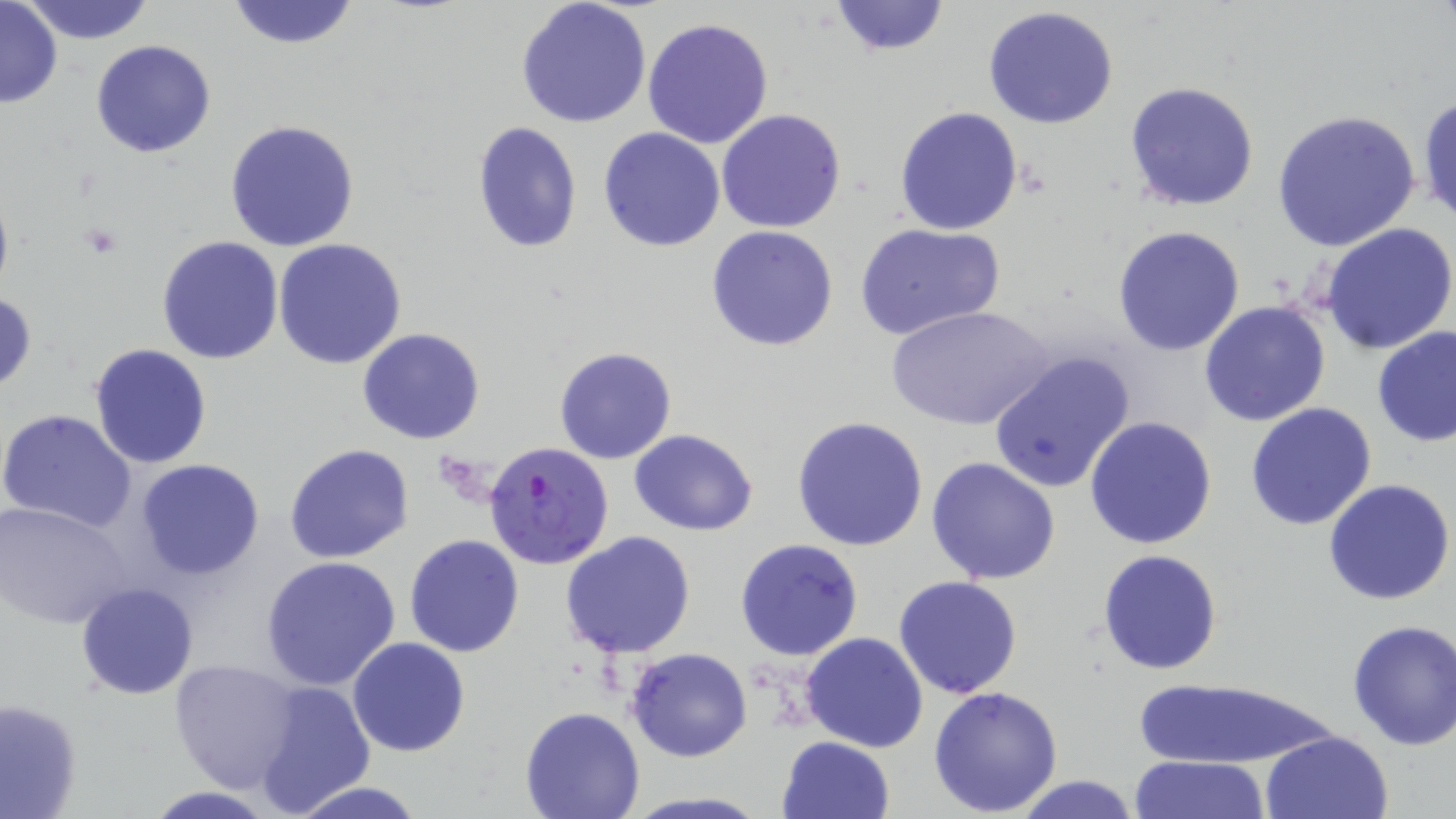

Summary:
  - Coordinate format: approximate bounding boxes as [x1, y1, x2, y2] in pixels
  - Uninfected red blood cell locations: [0, 0, 63, 110], [23, 0, 155, 44], [224, 0, 361, 50], [826, 0, 952, 56], [515, 1, 653, 128], [982, 6, 1121, 129], [642, 17, 773, 148], [90, 39, 217, 158], [1124, 81, 1260, 212], [1417, 93, 1456, 228], [895, 106, 1023, 234], [716, 108, 846, 233], [1273, 110, 1422, 253], [225, 119, 361, 252], [471, 122, 582, 252], [599, 127, 726, 251], [854, 222, 1006, 342], [1321, 222, 1456, 355], [1112, 224, 1245, 356], [706, 226, 839, 351], [157, 235, 285, 364], [274, 239, 408, 370], [1, 292, 37, 396], [1198, 300, 1332, 426], [889, 306, 1054, 433], [1372, 326, 1456, 447], [358, 328, 486, 445], [89, 343, 213, 467], [552, 347, 677, 465], [985, 349, 1136, 497], [1244, 402, 1377, 531], [0, 408, 138, 533], [791, 415, 928, 553], [1084, 415, 1217, 551], [629, 426, 759, 537], [284, 443, 414, 565], [926, 456, 1061, 586], [133, 459, 265, 579], [1323, 479, 1455, 606], [1, 499, 135, 629], [558, 531, 698, 659], [404, 534, 525, 659], [734, 538, 864, 661], [1097, 549, 1223, 675], [259, 555, 403, 691], [893, 575, 1023, 699], [75, 581, 198, 700], [1346, 618, 1456, 751], [801, 631, 929, 753], [347, 636, 471, 756], [626, 646, 753, 763], [167, 659, 301, 794], [1136, 678, 1335, 771], [251, 680, 375, 816], [929, 685, 1064, 815], [0, 698, 83, 819], [519, 707, 645, 819], [1261, 730, 1393, 818], [777, 736, 896, 819], [1128, 754, 1274, 818], [1010, 774, 1145, 818], [285, 781, 427, 819], [142, 786, 280, 819], [621, 791, 774, 819]
  - Platelet locations: [76, 223, 126, 259], [436, 452, 498, 504]
  - Plasmodium falciparum-infected red blood cell locations: [484, 441, 613, 571]
  - Slide-level diagnosis: Plasmodium falciparum
  - Modality: light microscopy
  - Magnification: 1000x
  - Stain: May-Grünwald-Giemsa
  - Preparation: thin blood film
  - Image size: 1456×819 pixels
  - Field of view: single